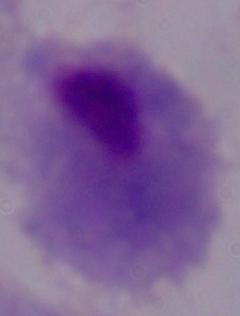

identification: trichomonad
magnification: 1000x
modality: photomicrograph